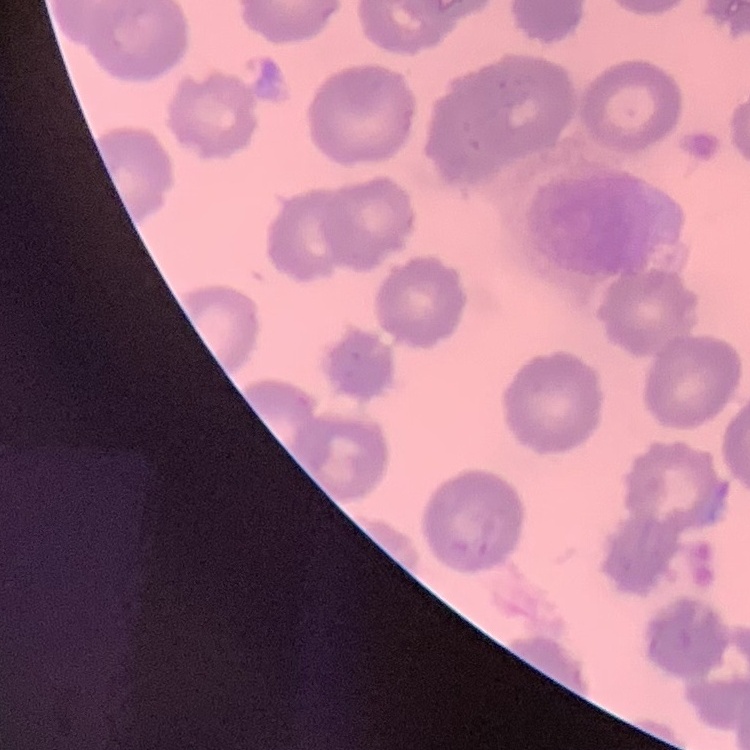 The red blood cells exhibit no rouleaux formation. Thin blood film. One tile cut from a larger photomicrograph. Field's or Giemsa stain.